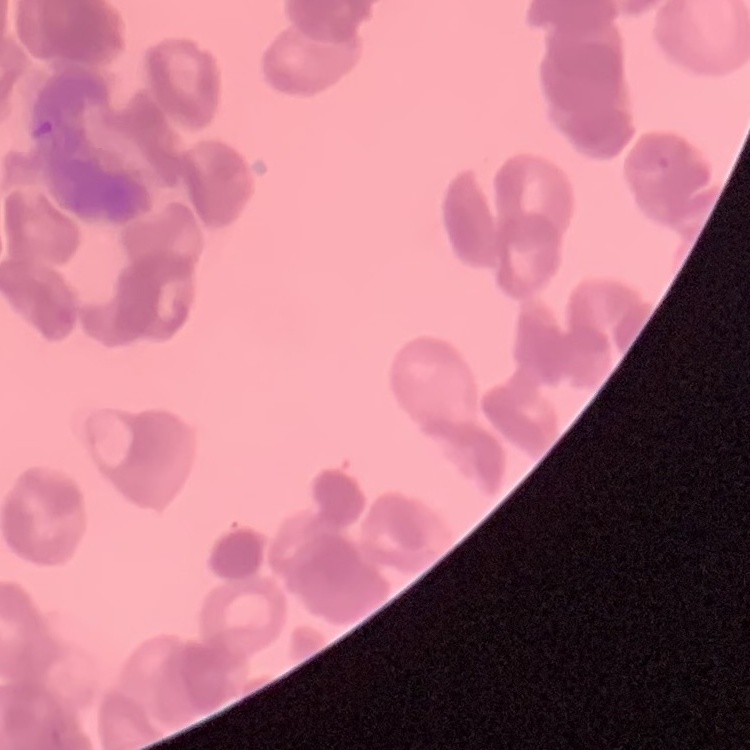

The erythrocytes exhibit rouleaux formation. Thin blood film. Stained with either Field's or Giemsa. One tile cut from a larger photomicrograph.